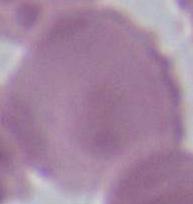
Summary:
  - Identification: erythrocyte
  - Modality: micrograph
  - Magnification: 1000x